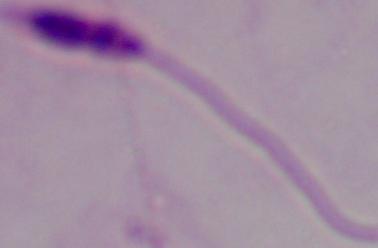
magnification: 1000x
identification: Leishmania
modality: micrograph